Classify this cell by malaria status.
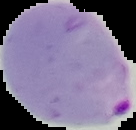
It is parasitized.

{
  "image_size": "136×130 pixels",
  "image_type": "segmented cell region with the area outside set to black",
  "preparation": "thin blood smear"
}